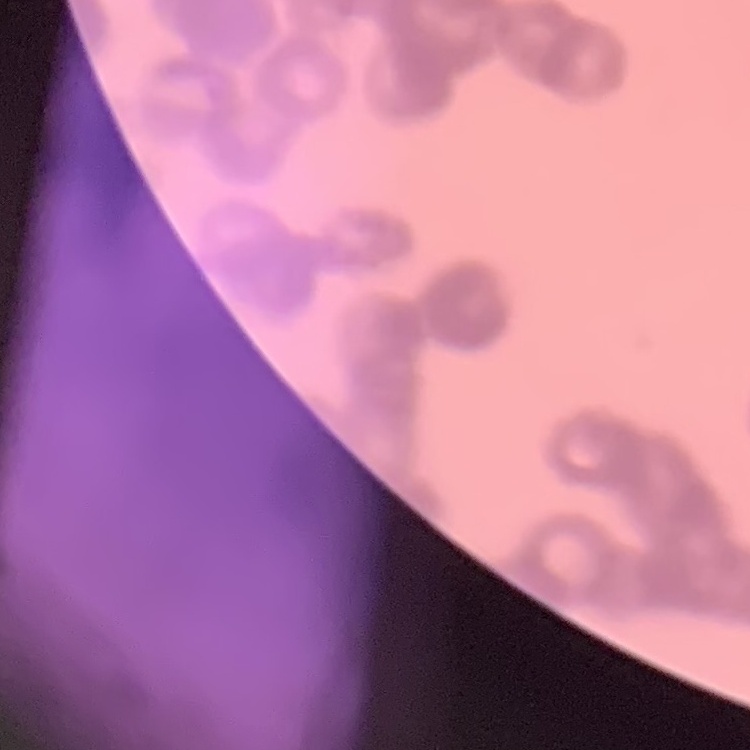

The erythrocytes show rouleaux formation. Square crop of a larger photomicrograph. Thin peripheral smear. Stained with either Field's or Giemsa.